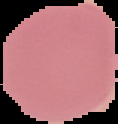
Summary:
  - Preparation: thin blood film
  - Image size: 118×124 pixels
  - Image type: segmented cell region with the area outside set to black
  - Malaria status: uninfected